Describe the morphology of the erythrocytes.
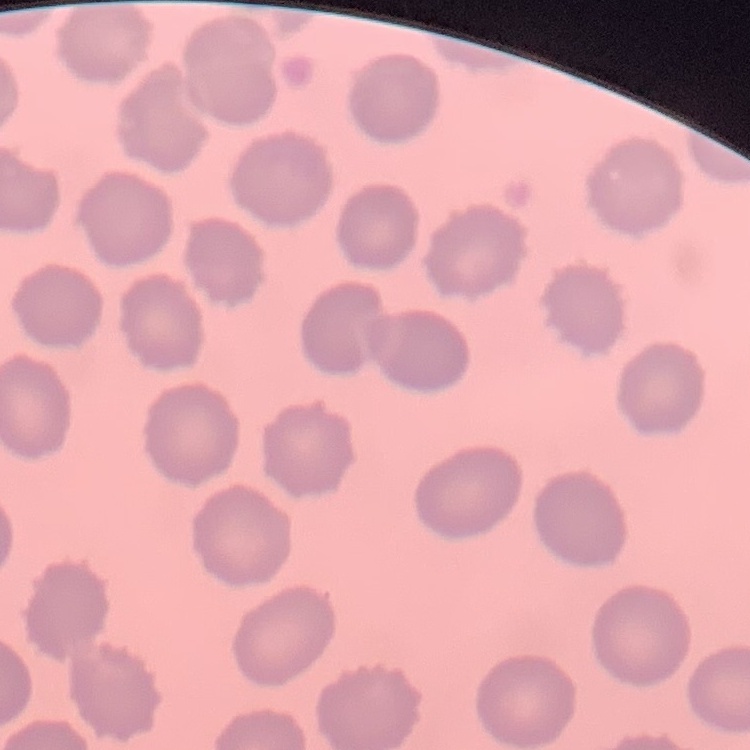
No rouleaux formation.

stain = Field's or Giemsa
preparation = thin blood film
image type = square crop of a larger photomicrograph